Assess this cell for malaria.
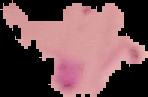
It is parasitized.

The area outside the segmented cell region is set to black. Image is 148×97 pixels. From a thin blood film.